Report the malaria status of this cell.
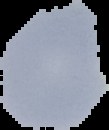

Uninfected.

image type = segmented cell region with the area outside set to black
image size = 109×130 pixels
preparation = thin blood film